Give the position of every malaria parasite.
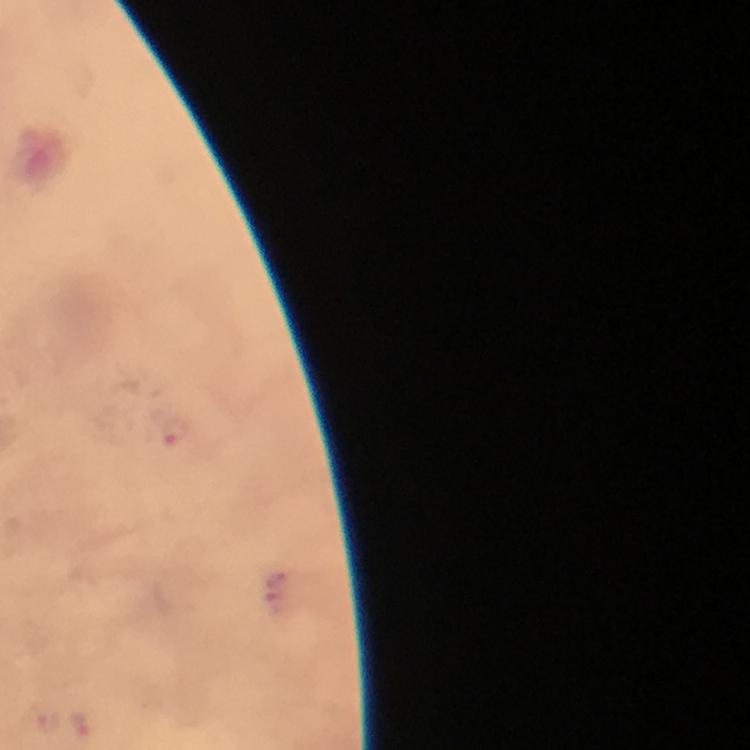

Approximate centers as [x, y] in pixels.
Malaria parasites: [175, 432].

Summary:
  - Context: from a diagnostic examination for malaria
  - Cropped from: a single field of view
  - Stain: Giemsa
  - Capture: smartphone camera through the microscope
  - Magnification: 100x
  - Image size: 750×750 pixels
  - Preparation: thick smear
  - Immersion oil: used